Report the malaria status of this cell.
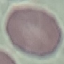
Uninfected.

Summary:
  - Capture: smartphone camera at the microscope eyepiece
  - Stain: Giemsa
  - Image type: automatically extracted cell patch, resized to 64 × 64 pixels
  - Preparation: thin smear